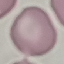

result = no malaria parasites detected
stain = Giemsa
preparation = thin blood smear
capture = smartphone camera at the microscope eyepiece
image type = cell patch, automatically extracted from a larger field of view and resized to 64 × 64 pixels